Comment on the morphology of the red blood cells.
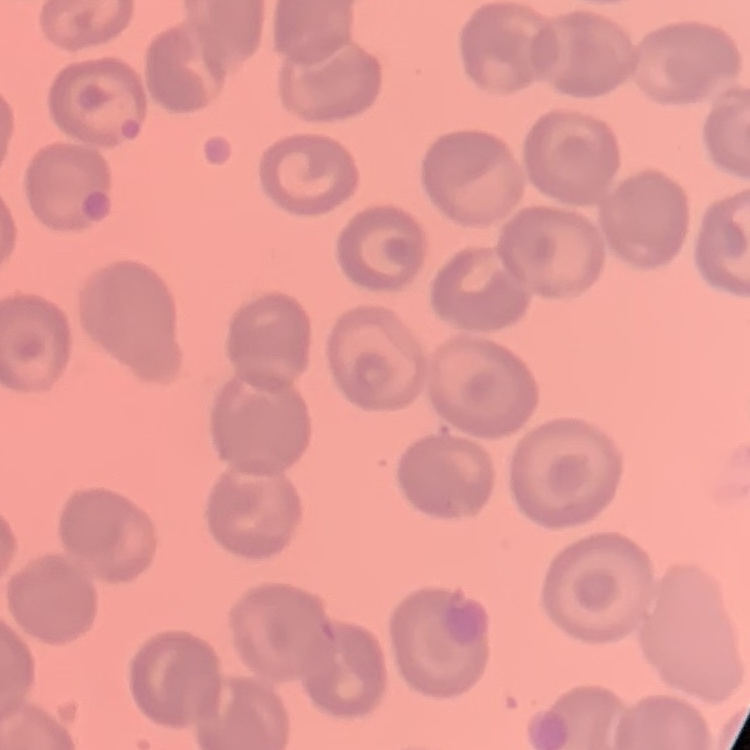

They show no rouleaux formation.

Stained with either Field's or Giemsa. Square crop of a larger photomicrograph. Thin blood smear.